Outline each blood parasite and name the species.
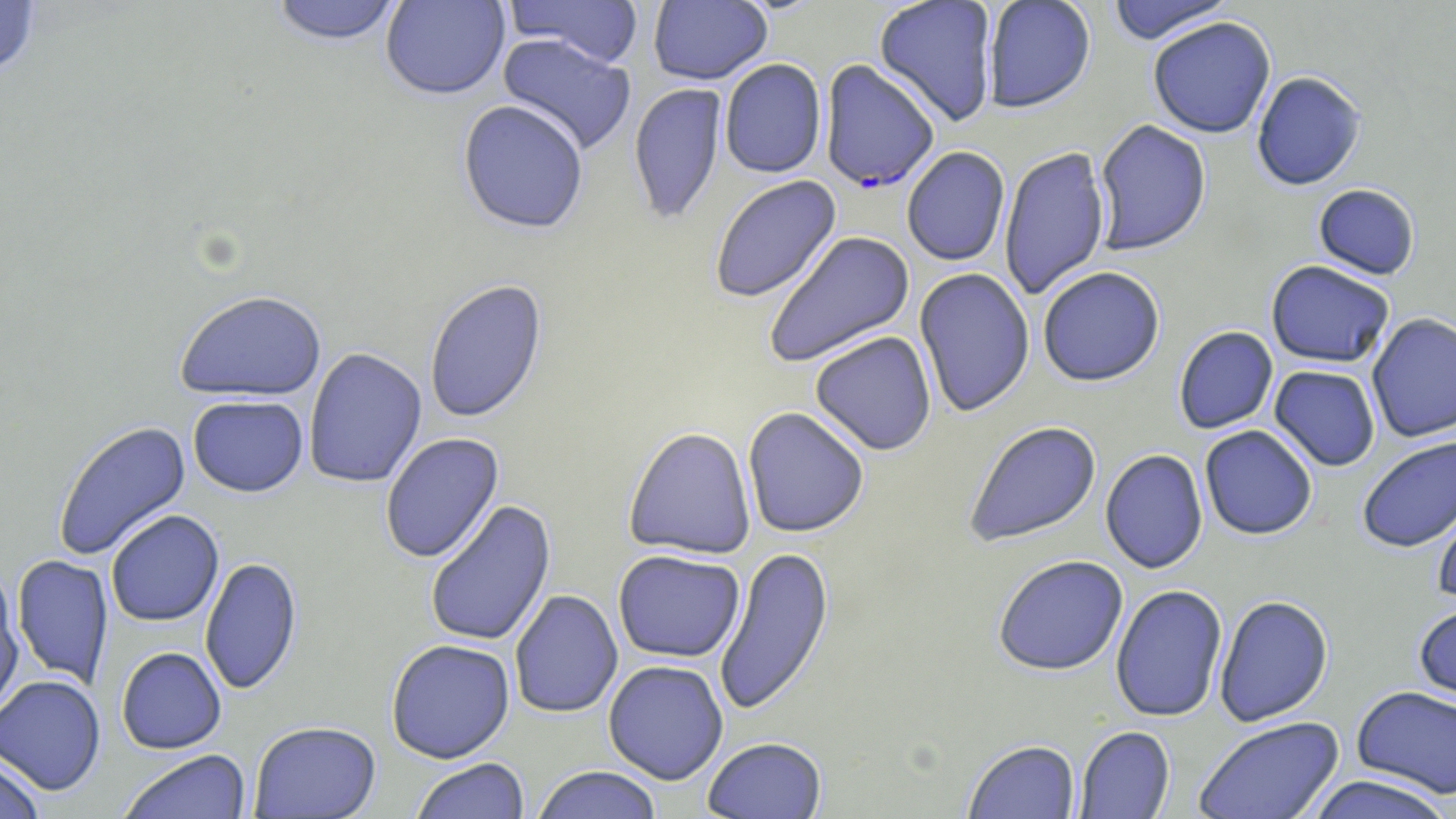
Approximate bounding boxes as (x1,y1)-(x2,y2) corner pairs in pixels.
Plasmodium falciparum-infected red blood cells: (819,59)-(940,194).
No Plasmodium ovale, Plasmodium malariae, Plasmodium vivax, Babesia divergens, or Trypanosoma brucei observed.

{
  "slide_level_diagnosis": "Plasmodium falciparum",
  "magnification": "1000x",
  "image_size": "1456×819 pixels",
  "field_of_view": "one of a larger specimen",
  "stain": "May-Grünwald-Giemsa",
  "modality": "optical microscopy",
  "uninfected_red_blood_cell_locations": "approximate bounding boxes as (x1,y1)-(x2,y2) corner pairs in pixels: (268,0)-(404,48), (380,0)-(510,101), (504,0)-(644,69), (648,0)-(772,86), (874,0)-(999,127), (982,0)-(1096,114), (0,1)-(41,80), (1105,1)-(1238,45), (1147,16)-(1276,139), (497,33)-(637,156), (719,59)-(827,179), (1251,71)-(1367,191), (628,83)-(727,224), (457,100)-(589,235), (1094,119)-(1211,256), (901,146)-(1011,266), (999,146)-(1111,301), (709,175)-(842,304), (1313,184)-(1420,280), (763,230)-(915,369), (1265,260)-(1395,369), (1038,266)-(1165,387), (914,268)-(1035,418), (424,279)-(548,424), (174,289)-(327,402), (1366,313)-(1456,443), (1173,326)-(1278,434), (810,331)-(937,456), (303,347)-(427,489), (1269,365)-(1381,472), (187,395)-(308,497), (742,407)-(870,538), (52,420)-(191,562), (964,420)-(1102,549), (1199,424)-(1318,540), (623,426)-(757,561), (380,432)-(504,564), (1356,435)-(1456,553), (1100,449)-(1208,574), (1430,484)-(1456,606), (424,499)-(556,647), (105,509)-(224,627), (714,545)-(835,717), (613,550)-(745,663), (12,555)-(114,689), (200,555)-(303,696), (992,555)-(1128,676), (0,576)-(24,718), (1110,584)-(1228,722), (509,589)-(623,719), (1213,594)-(1333,726), (1413,597)-(1456,710), (385,639)-(515,763), (116,646)-(227,754), (603,660)-(729,784), (0,674)-(106,795), (1351,685)-(1456,799), (1193,716)-(1345,819), (248,720)-(382,818), (1075,726)-(1175,818), (702,737)-(828,819), (963,739)-(1081,818), (117,749)-(251,819), (0,756)-(45,819), (409,758)-(529,818), (531,765)-(664,819), (1303,774)-(1455,819)",
  "preparation": "thin blood smear"
}